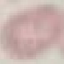
Summary:
  - Malaria status: uninfected
  - Image type: cell patch, automatically extracted from a larger field of view and resized to 64 × 64 pixels
  - Preparation: thin blood film
  - Stain: Giemsa
  - Capture: smartphone through the microscope eyepiece